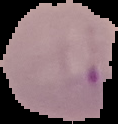 From a thin blood smear. Segmented cell region on a black background. Result: Plasmodium parasites identified. Image is 118×124 pixels.